State which parasite is depicted.
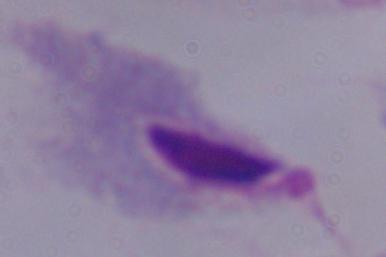

This is a trichomonad.

modality = photomicrograph
magnification = 1000x